Classify this cell by malaria status.
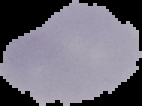

It is uninfected.

Image is 142×106 pixels. From a thin blood film. Segmented cell region on a black background.